Report the malaria status of this cell.
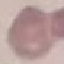

It is uninfected.

Summary:
  - Preparation: thin blood film
  - Capture: smartphone through the microscope eyepiece
  - Image type: cell patch, automatically extracted from a larger field of view and resized to 64 × 64 pixels
  - Stain: Giemsa